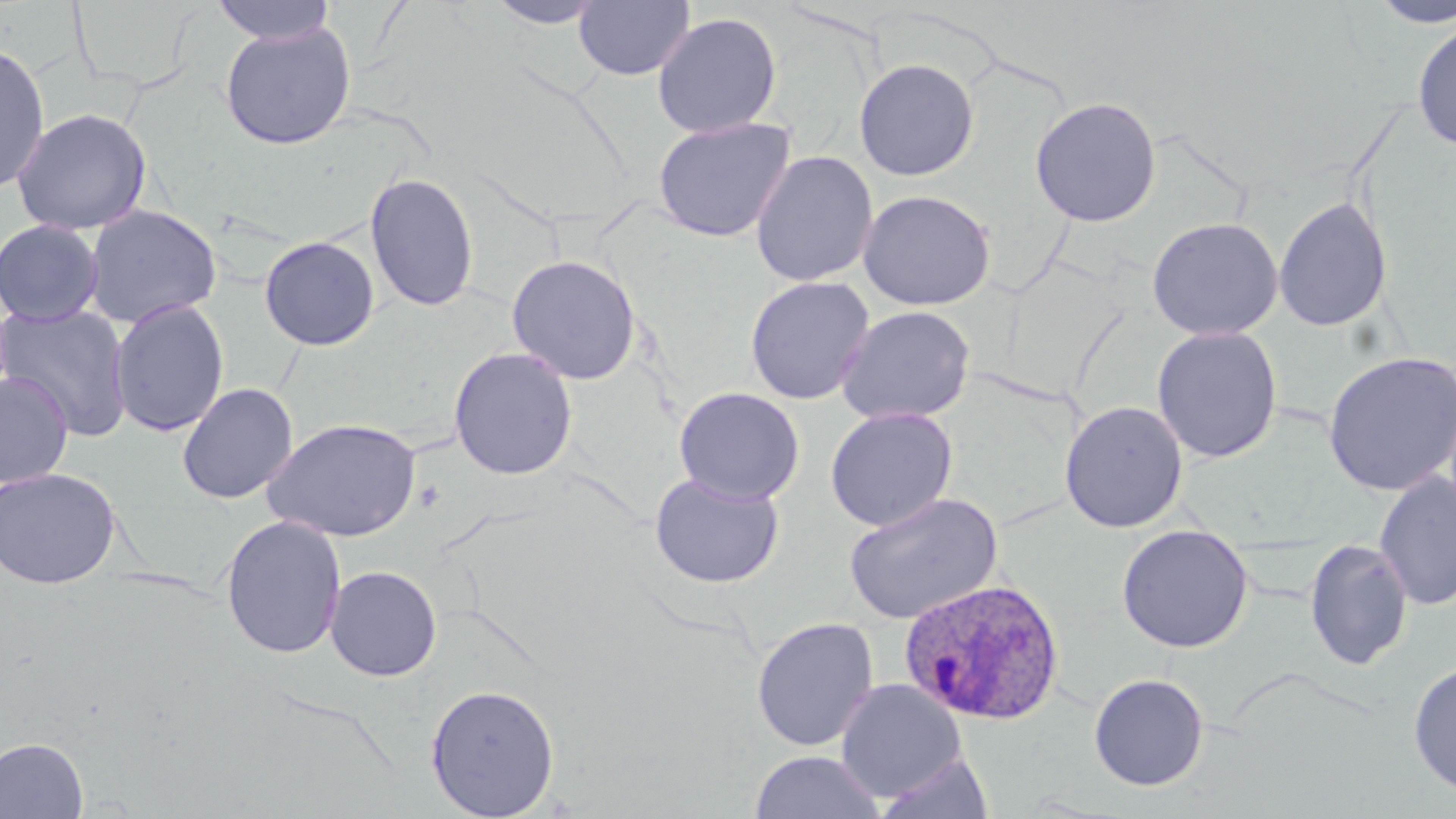

Summary:
  - Coordinate format: approximate bounding boxes as (x1,y1)-(x2,y2) corner pairs in pixels
  - Uninfected red blood cell locations: (210,0)-(337,45), (483,0)-(610,29), (573,1)-(695,81), (1369,1)-(1456,29), (651,11)-(783,138), (219,20)-(357,149), (1412,20)-(1456,154), (0,41)-(51,194), (853,57)-(980,181), (1029,96)-(1162,227), (11,107)-(152,235), (652,116)-(797,242), (750,150)-(879,287), (364,171)-(480,313), (857,189)-(997,311), (1273,196)-(1393,332), (83,204)-(222,328), (1146,216)-(1284,341), (0,219)-(105,327), (258,235)-(380,351), (506,253)-(643,385), (744,276)-(875,406), (108,298)-(230,437), (0,303)-(134,442), (835,305)-(976,426), (1151,326)-(1283,463), (448,346)-(579,481), (1322,351)-(1455,497), (1,371)-(75,489), (176,382)-(299,504), (673,386)-(805,505), (1059,400)-(1188,533), (825,406)-(958,532), (262,418)-(422,542), (0,466)-(122,589), (1374,471)-(1456,611), (649,472)-(784,589), (843,491)-(1003,625), (220,515)-(347,660), (1115,524)-(1254,653), (1304,538)-(1413,671), (324,564)-(443,682), (751,616)-(879,752), (1408,660)-(1456,798), (1088,672)-(1210,791), (835,679)-(967,803), (425,682)-(560,818), (0,737)-(89,818), (749,750)-(886,819), (876,751)-(993,818)
  - Plasmodium ovale-infected red blood cell locations: (898,576)-(1066,725)
  - Slide-level diagnosis: Plasmodium ovale
  - Field of view: single
  - Stain: May-Grünwald-Giemsa
  - Preparation: thin blood film
  - Image size: 1456×819 pixels
  - Modality: optical microscopy
  - Magnification: 1000x